Give the extent of all Plasmodium falciparum-infected red blood cells.
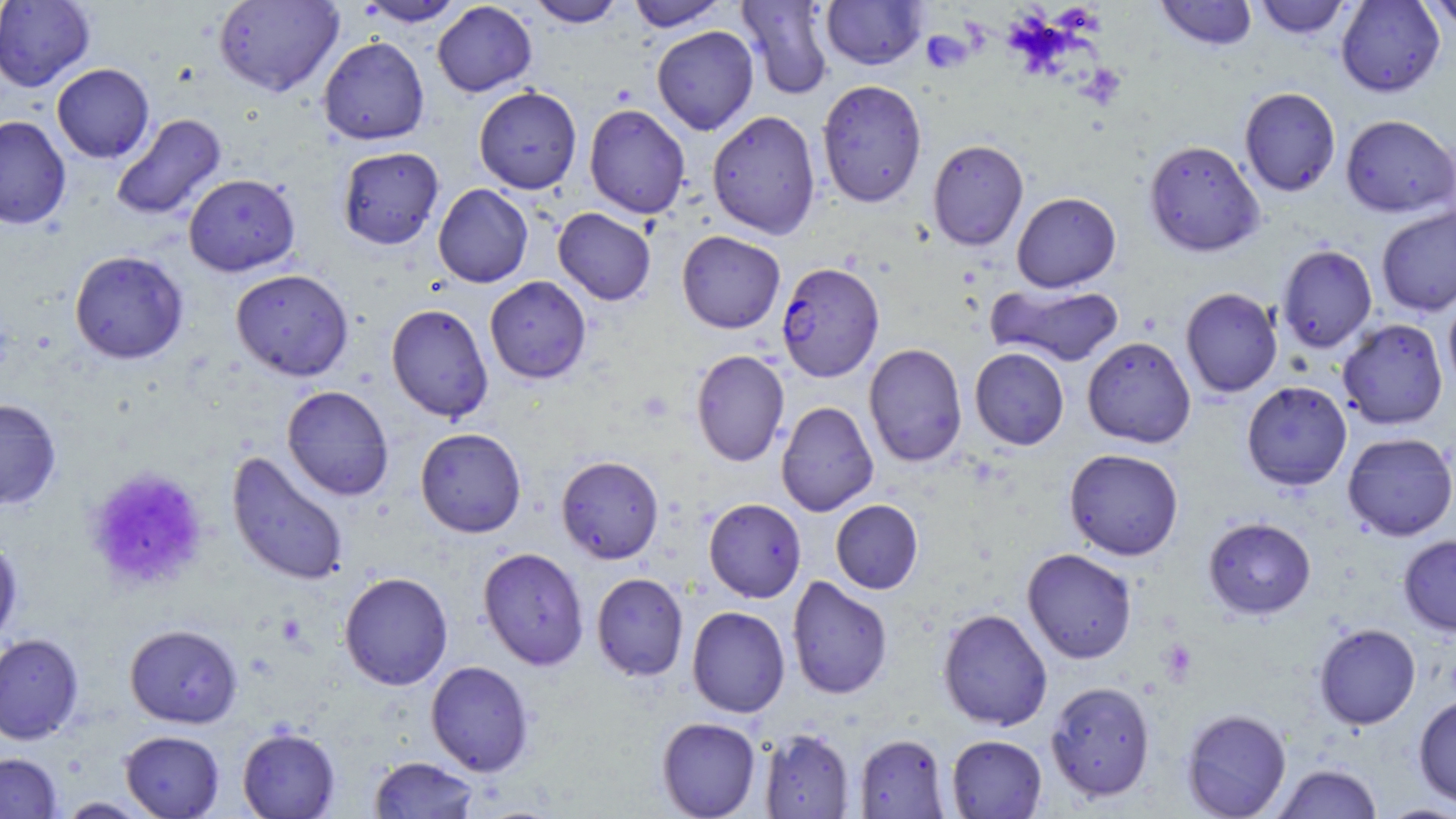

Approximate bounding boxes as (x1, y1, x2, y2) in pixels.
Plasmodium falciparum-infected red blood cells: (776, 261, 884, 382).

Summary:
  - Platelet locations: (921, 31, 971, 72), (84, 467, 208, 592), (1158, 639, 1198, 685)
  - Uninfected red blood cell locations: (0, 0, 96, 91), (213, 0, 343, 97), (354, 0, 468, 26), (526, 0, 626, 28), (625, 0, 730, 30), (820, 0, 927, 69), (1154, 0, 1257, 50), (1253, 0, 1353, 38), (1335, 0, 1445, 97), (1421, 0, 1456, 32), (432, 1, 537, 97), (736, 1, 836, 100), (652, 26, 759, 135), (317, 37, 430, 145), (52, 63, 155, 163), (816, 79, 927, 208), (474, 86, 582, 194), (1239, 87, 1340, 196), (584, 104, 691, 219), (707, 110, 821, 239), (110, 113, 226, 221), (1340, 114, 1455, 217), (0, 116, 71, 229), (927, 139, 1028, 250), (1144, 139, 1264, 257), (337, 146, 444, 250), (183, 173, 300, 276), (433, 184, 533, 288), (1011, 191, 1121, 292), (1376, 206, 1456, 316), (553, 208, 656, 305), (677, 230, 785, 334), (1277, 244, 1377, 352), (69, 250, 189, 364), (231, 268, 354, 381), (484, 276, 592, 384), (988, 282, 1125, 367), (1180, 287, 1283, 398), (1443, 294, 1456, 398), (386, 303, 493, 423), (1337, 318, 1448, 430), (1082, 336, 1196, 448), (863, 342, 968, 467), (969, 347, 1069, 450), (691, 350, 790, 467), (1242, 381, 1352, 490), (281, 385, 394, 501), (0, 398, 61, 509), (776, 401, 878, 517), (415, 427, 527, 537), (1342, 432, 1456, 541), (1064, 448, 1184, 560), (227, 451, 349, 587), (556, 455, 664, 564), (697, 497, 799, 720), (703, 498, 806, 602), (830, 499, 923, 594), (1203, 516, 1316, 618), (1398, 534, 1456, 636), (0, 537, 23, 646), (477, 547, 589, 670), (1022, 547, 1137, 664), (339, 571, 453, 690), (591, 573, 688, 681), (786, 575, 893, 700), (687, 606, 790, 718), (937, 608, 1052, 731), (1314, 623, 1420, 729), (125, 624, 243, 728), (0, 633, 84, 744), (425, 661, 534, 776), (1045, 680, 1156, 802), (1413, 694, 1456, 809), (1181, 708, 1291, 819), (656, 717, 761, 818), (237, 727, 340, 819), (759, 728, 854, 818), (120, 730, 225, 818), (855, 733, 950, 818), (946, 734, 1047, 818), (0, 752, 62, 818), (368, 756, 481, 818), (1272, 763, 1383, 818), (54, 797, 153, 818), (1375, 803, 1456, 818)
  - Slide-level diagnosis: Plasmodium falciparum
  - Magnification: 1000x
  - Image size: 1456×819 pixels
  - Modality: optical microscopy
  - Preparation: thin blood smear
  - Field of view: one of a larger specimen
  - Stain: May-Grünwald-Giemsa